Locate and identify every blood parasite.
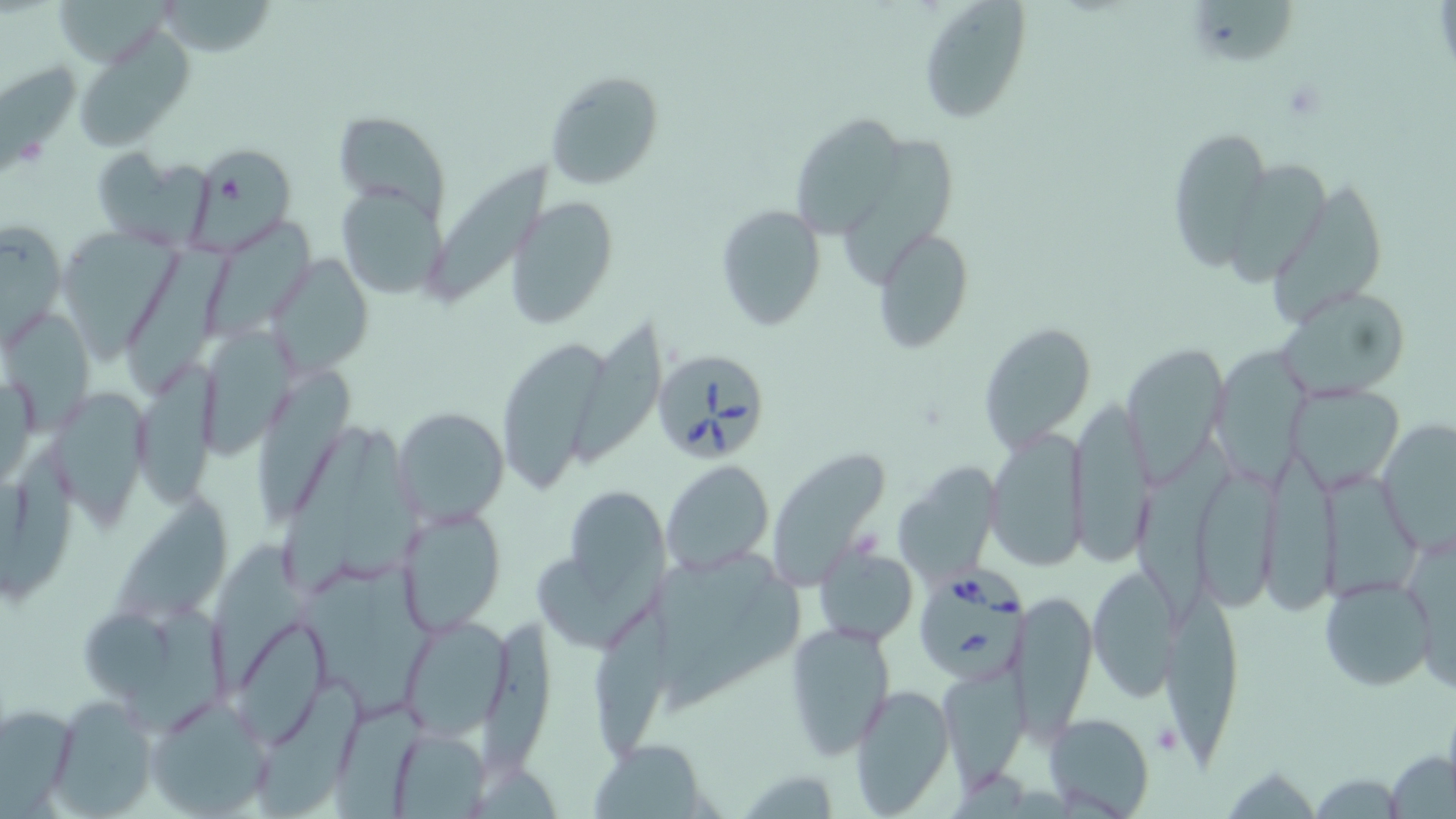

Approximate bounding boxes as [x1, y1, x2, y2] in pixels.
Babesia divergens-infected red blood cells: [658, 352, 768, 459], [914, 574, 1026, 683].
No Plasmodium falciparum, Plasmodium ovale, Plasmodium malariae, Plasmodium vivax, or Trypanosoma brucei observed.

slide_level_diagnosis: Babesia divergens
platelet_locations: 'approximate bounding boxes as [x1, y1, x2, y2] in pixels: [1153, 722, 1183, 755]'
stain: May-Grünwald-Giemsa
image_size: 1456×819 pixels
modality: optical microscopy
field_of_view: single
uninfected_red_blood_cell_locations: 'approximate bounding boxes as [x1, y1, x2, y2] in pixels: [50, 0, 165, 65], [918, 0, 1031, 123], [155, 1, 275, 57], [1196, 2, 1302, 69], [74, 28, 193, 150], [0, 63, 81, 172], [544, 68, 665, 190], [331, 108, 450, 216], [794, 113, 891, 235], [1166, 125, 1274, 270], [849, 132, 953, 280], [187, 143, 295, 250], [90, 148, 213, 248], [425, 162, 552, 295], [1235, 164, 1328, 286], [1262, 173, 1383, 322], [335, 180, 448, 300], [505, 197, 620, 330], [716, 203, 825, 331], [1, 216, 68, 348], [206, 219, 317, 337], [62, 228, 182, 355], [875, 228, 973, 351], [130, 238, 222, 385], [267, 253, 374, 377], [1273, 285, 1410, 402], [5, 304, 102, 443], [567, 322, 671, 469], [977, 322, 1099, 452], [197, 326, 299, 459], [493, 333, 614, 494], [1215, 339, 1305, 482], [1120, 342, 1227, 485], [133, 362, 218, 507], [255, 370, 352, 531], [1284, 380, 1406, 496], [47, 386, 149, 526], [1068, 395, 1156, 566], [393, 404, 509, 526], [1380, 419, 1456, 551], [345, 428, 424, 577], [985, 428, 1087, 569], [281, 430, 371, 601], [1140, 434, 1231, 634], [1, 441, 74, 605], [770, 449, 891, 586], [1264, 455, 1341, 615], [662, 460, 774, 577], [1316, 464, 1422, 608], [1201, 465, 1281, 614], [896, 466, 998, 586], [559, 482, 669, 602], [111, 491, 229, 627], [395, 503, 509, 636], [217, 538, 311, 691], [815, 542, 919, 649], [663, 554, 809, 717], [539, 560, 671, 646], [305, 567, 435, 717], [1086, 567, 1178, 702], [1318, 576, 1435, 692], [1158, 585, 1243, 762], [1011, 587, 1098, 733], [136, 593, 231, 731], [592, 602, 681, 762], [75, 603, 174, 699], [399, 615, 513, 739], [228, 616, 331, 747], [483, 618, 559, 777], [785, 621, 895, 763], [938, 667, 1030, 786], [255, 679, 366, 815], [848, 682, 955, 814], [43, 696, 156, 817], [147, 696, 273, 817], [0, 702, 78, 814], [332, 703, 429, 819], [1044, 712, 1154, 818], [387, 726, 493, 817], [589, 739, 708, 819], [1385, 749, 1455, 819], [1229, 771, 1310, 818], [1315, 772, 1398, 818]'
magnification: 1000x
preparation: thin blood film